Identify the cell.
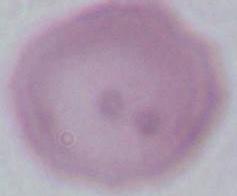

An erythrocyte.

Summary:
  - Magnification: 1000x
  - Modality: photomicrograph